Name the parasite shown.
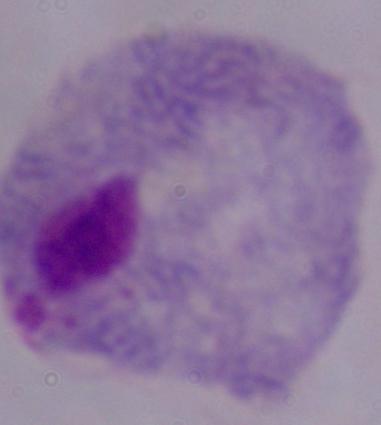
A trichomonad.

Micrograph. 1000x magnification.